Classify this cell by malaria status.
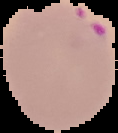

Parasitized.

Summary:
  - Image type: cell region segmented out of the field of view; surrounding area masked to black
  - Preparation: thin blood film
  - Image size: 118×133 pixels